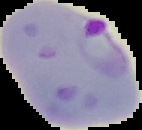

Segmented cell region on a black background. From a thin blood film. Image is 142×130 pixels. Malaria status: parasitized.